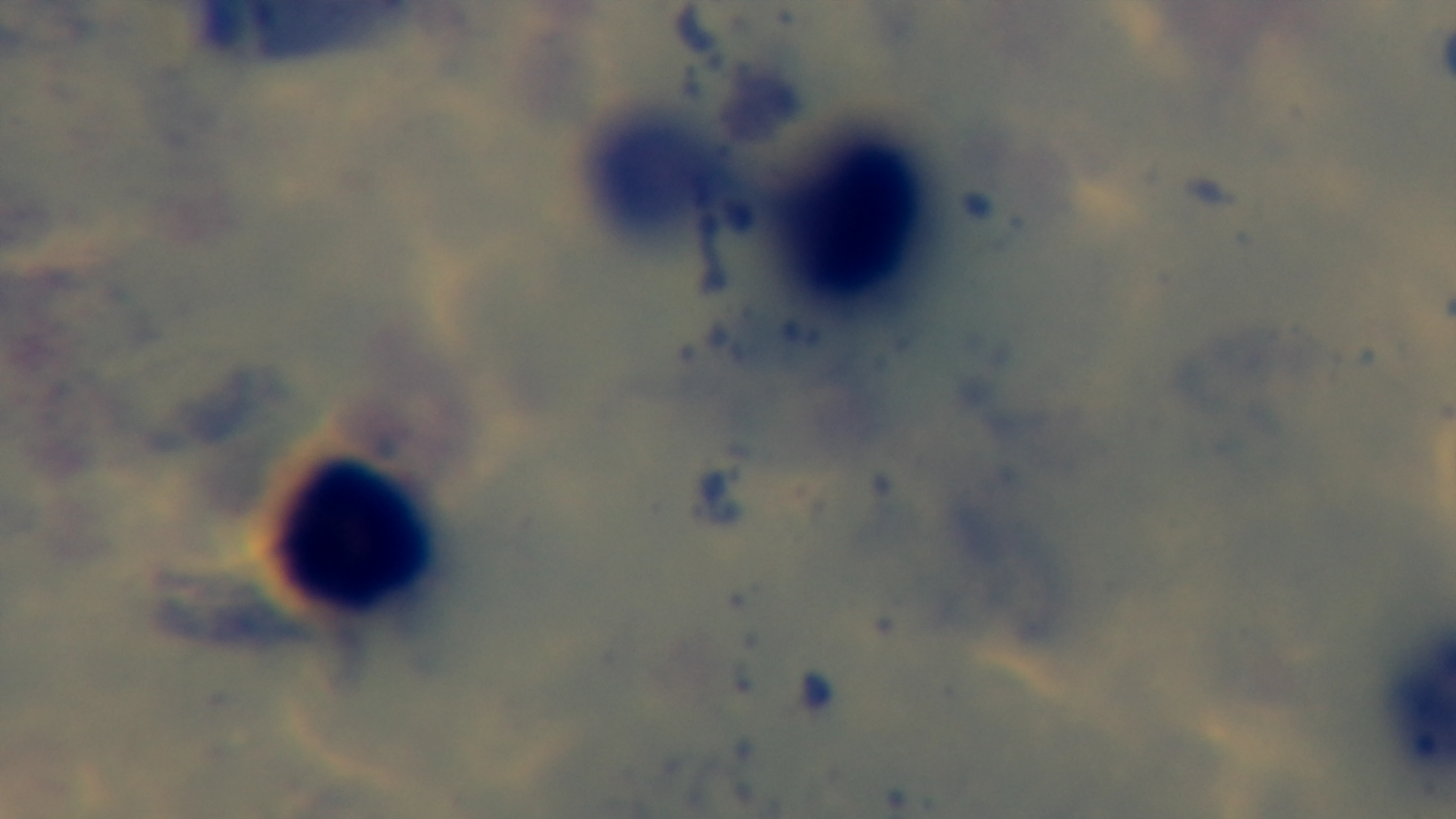

Summary:
  - Modality: light microscopy
  - Field of view: one from the slide
  - Stain: Giemsa
  - Capture: mounted 4K digital camera
  - Malaria status: negative
  - Objective: 100x oil immersion
  - Preparation: thick blood film